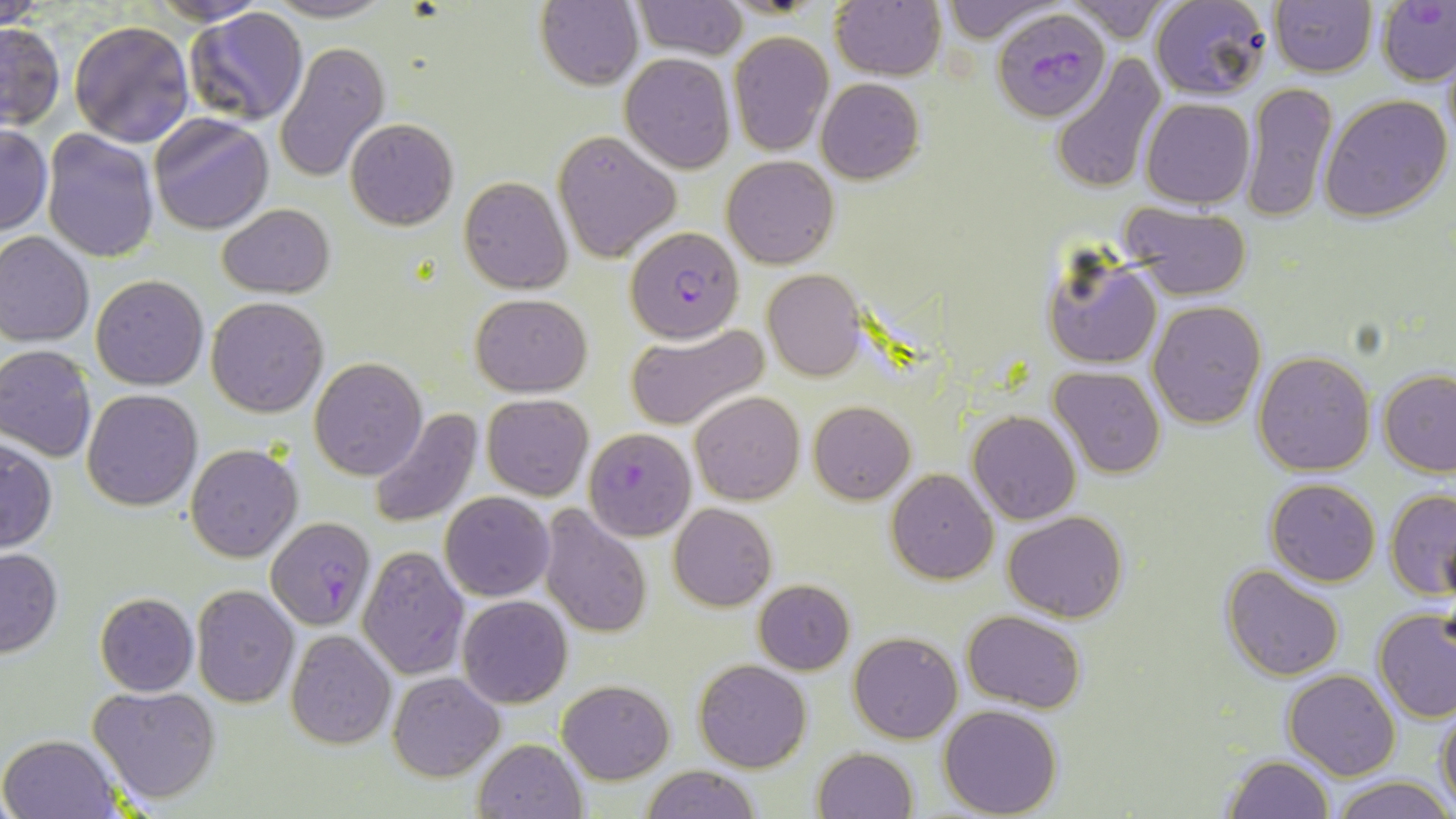

Summary:
  - Coordinate format: approximate bounding boxes as named x1/y1/x2/y2 corners in pixels
  - Uninfected red blood cell locations: (x1=0, y1=0, x2=46, y2=28), (x1=146, y1=0, x2=278, y2=25), (x1=264, y1=0, x2=393, y2=23), (x1=536, y1=0, x2=644, y2=90), (x1=632, y1=0, x2=748, y2=60), (x1=935, y1=0, x2=1066, y2=42), (x1=1149, y1=0, x2=1273, y2=101), (x1=830, y1=2, x2=946, y2=80), (x1=1062, y1=2, x2=1174, y2=44), (x1=1268, y1=2, x2=1377, y2=77), (x1=183, y1=8, x2=311, y2=128), (x1=69, y1=19, x2=195, y2=147), (x1=0, y1=21, x2=65, y2=130), (x1=728, y1=30, x2=833, y2=156), (x1=275, y1=41, x2=390, y2=182), (x1=1050, y1=52, x2=1167, y2=193), (x1=619, y1=54, x2=736, y2=174), (x1=815, y1=77, x2=925, y2=185), (x1=1242, y1=82, x2=1337, y2=222), (x1=1319, y1=94, x2=1453, y2=222), (x1=1141, y1=97, x2=1254, y2=206), (x1=149, y1=113, x2=274, y2=235), (x1=345, y1=118, x2=458, y2=230), (x1=0, y1=124, x2=51, y2=237), (x1=41, y1=129, x2=159, y2=263), (x1=552, y1=129, x2=681, y2=264), (x1=722, y1=155, x2=840, y2=269), (x1=458, y1=176, x2=571, y2=294), (x1=217, y1=204, x2=336, y2=297), (x1=1120, y1=204, x2=1252, y2=300), (x1=0, y1=231, x2=96, y2=346), (x1=1044, y1=249, x2=1163, y2=370), (x1=762, y1=267, x2=866, y2=381), (x1=91, y1=275, x2=209, y2=390), (x1=471, y1=292, x2=592, y2=396), (x1=205, y1=296, x2=329, y2=418), (x1=1148, y1=300, x2=1267, y2=428), (x1=624, y1=321, x2=772, y2=432), (x1=0, y1=345, x2=98, y2=462), (x1=1253, y1=350, x2=1376, y2=475), (x1=309, y1=356, x2=427, y2=480), (x1=1047, y1=365, x2=1165, y2=479), (x1=1379, y1=368, x2=1456, y2=475), (x1=81, y1=388, x2=203, y2=511), (x1=689, y1=390, x2=805, y2=505), (x1=482, y1=394, x2=594, y2=501), (x1=808, y1=401, x2=915, y2=503), (x1=371, y1=408, x2=483, y2=526), (x1=968, y1=411, x2=1080, y2=525), (x1=0, y1=436, x2=56, y2=554), (x1=186, y1=443, x2=303, y2=563), (x1=886, y1=468, x2=997, y2=583), (x1=1264, y1=478, x2=1381, y2=585), (x1=1387, y1=488, x2=1456, y2=598), (x1=440, y1=491, x2=554, y2=602), (x1=668, y1=503, x2=777, y2=611), (x1=538, y1=506, x2=652, y2=637), (x1=1002, y1=510, x2=1129, y2=621), (x1=355, y1=545, x2=469, y2=680), (x1=0, y1=547, x2=63, y2=658), (x1=1221, y1=565, x2=1345, y2=681), (x1=753, y1=579, x2=854, y2=674), (x1=191, y1=584, x2=300, y2=710), (x1=94, y1=592, x2=199, y2=695), (x1=458, y1=595, x2=572, y2=707), (x1=1373, y1=608, x2=1456, y2=723), (x1=963, y1=611, x2=1086, y2=712), (x1=284, y1=629, x2=396, y2=749), (x1=850, y1=631, x2=962, y2=743), (x1=694, y1=658, x2=812, y2=772), (x1=1283, y1=669, x2=1400, y2=780), (x1=388, y1=670, x2=504, y2=781), (x1=557, y1=679, x2=674, y2=783), (x1=89, y1=685, x2=221, y2=804), (x1=1436, y1=702, x2=1456, y2=811), (x1=939, y1=705, x2=1064, y2=818), (x1=1, y1=733, x2=120, y2=819), (x1=473, y1=737, x2=588, y2=818), (x1=813, y1=746, x2=918, y2=819), (x1=1224, y1=755, x2=1336, y2=818), (x1=638, y1=766, x2=763, y2=819), (x1=1329, y1=774, x2=1456, y2=819)
  - Plasmodium falciparum-infected red blood cell locations: (x1=1377, y1=1, x2=1456, y2=87), (x1=992, y1=8, x2=1110, y2=124), (x1=624, y1=226, x2=746, y2=345), (x1=585, y1=428, x2=696, y2=539), (x1=266, y1=517, x2=376, y2=631)
  - Slide-level diagnosis: Plasmodium falciparum
  - Modality: optical microscopy
  - Stain: May-Grünwald-Giemsa
  - Field of view: one of a larger specimen
  - Image size: 1456×819 pixels
  - Preparation: thin blood smear
  - Magnification: 1000x